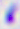

Summary:
  - Modality: photomicrograph
  - Magnification: 400x
  - Identification: Toxoplasma gondii